Assess the morphology of the red blood cells.
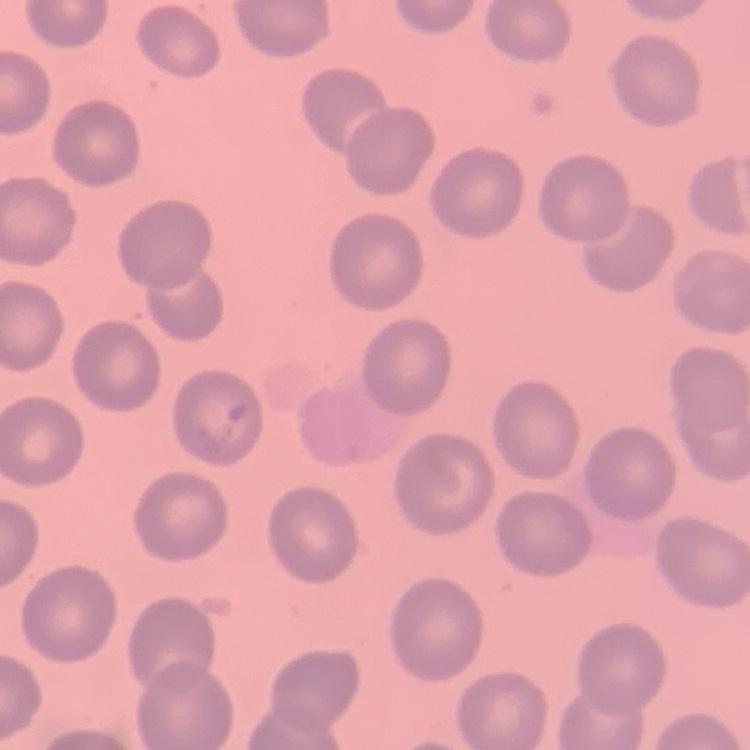

No rouleaux formation.

image_type: one tile cut from a larger photomicrograph
preparation: thin peripheral smear
stain: Field's or Giemsa